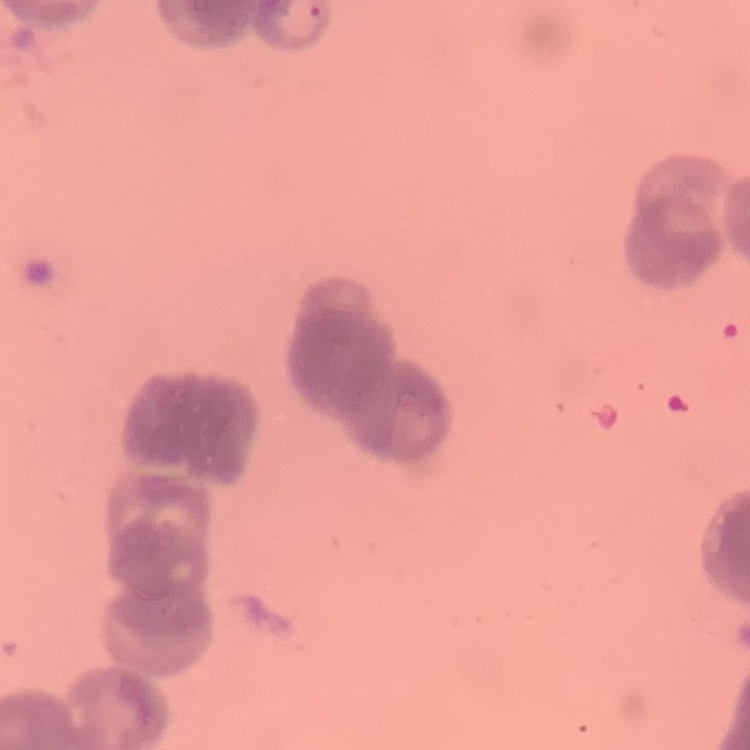
Summary:
  - Red blood cell morphology: rouleaux formation
  - Preparation: thin peripheral smear
  - Image type: square crop of a larger photomicrograph
  - Stain: Field's or Giemsa